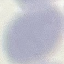

malaria status = uninfected
preparation = thin smear
capture = smartphone through the microscope eyepiece
stain = Giemsa
image type = cell patch, automatically extracted from a larger field of view and resized to 64 × 64 pixels